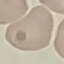
malaria status = uninfected
capture = smartphone through the microscope eyepiece
image type = automatically extracted cell patch, resized to 64 × 64 pixels
stain = Giemsa
preparation = thin blood smear